Identify the malaria species.
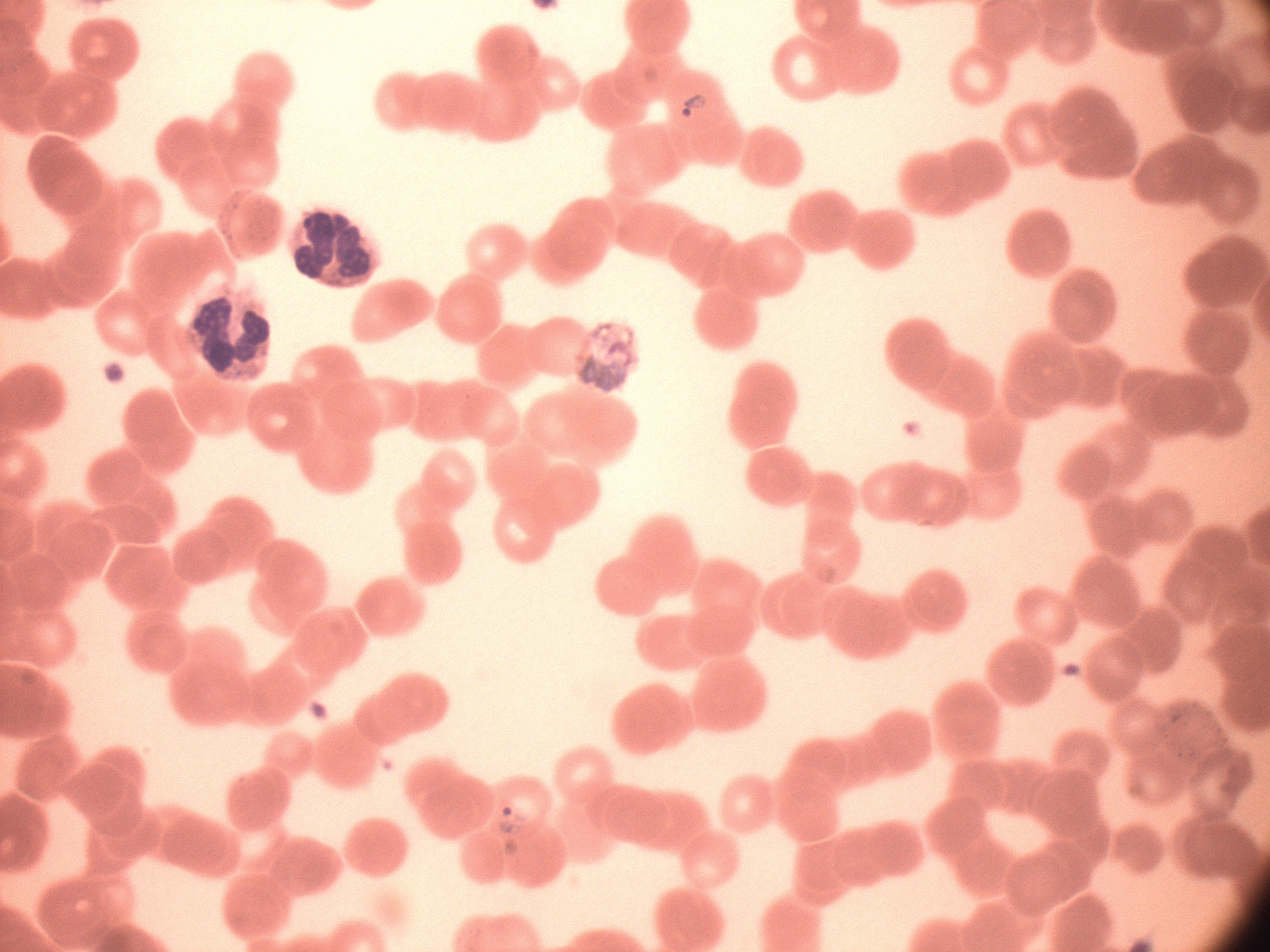

Plasmodium falciparum.

magnification = 100x
image size = 1270×952 pixels
preparation = thin blood film
ring form locations = approximate bounding boxes as [x1, y1, x2, y2] in pixels, from the source annotation, which is not necessarily exhaustive: [674, 85, 711, 125], [491, 800, 537, 840]
microscope = Leica DM2000 with built-in camera
field of view = single
stain = Giemsa